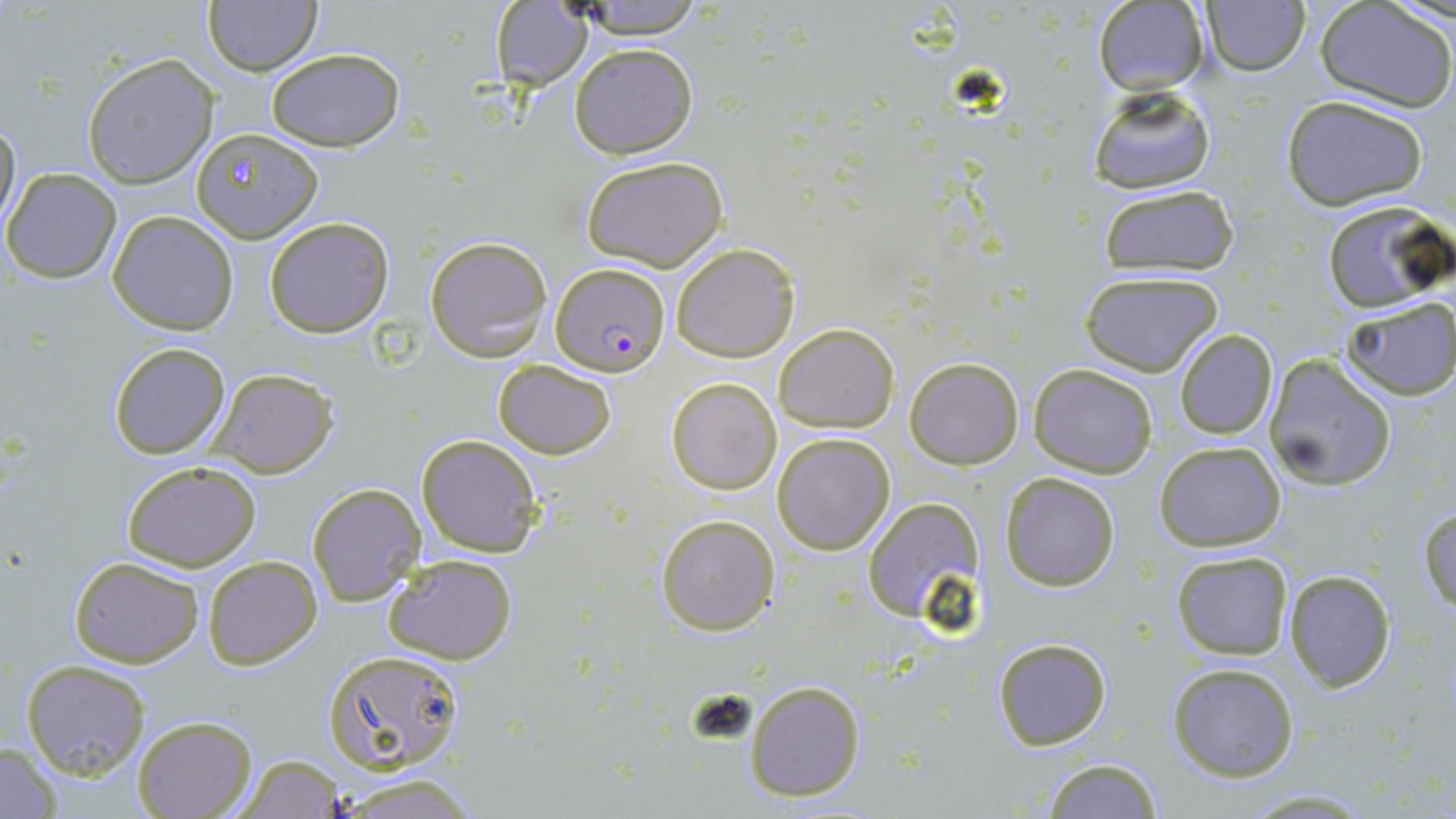
Approximate bounding boxes as [x1, y1, x2, y2] in pixels. Plasmodium falciparum-infected red blood cell locations: [548, 263, 669, 375]. Uninfected red blood cell locations: [1202, 0, 1308, 75], [203, 1, 321, 75], [570, 1, 709, 42], [489, 2, 594, 90], [1093, 2, 1210, 96], [1315, 2, 1454, 112], [570, 43, 698, 159], [263, 47, 408, 149], [83, 55, 218, 189], [1090, 86, 1215, 194], [1281, 94, 1430, 209], [0, 112, 21, 235], [190, 127, 321, 242], [581, 155, 730, 272], [2, 169, 121, 283], [1098, 182, 1240, 274], [1320, 200, 1450, 314], [107, 210, 239, 335], [263, 215, 395, 338], [425, 236, 551, 362], [672, 242, 800, 363], [1080, 271, 1224, 376], [1341, 298, 1456, 400], [774, 322, 900, 433], [1175, 329, 1277, 439], [106, 343, 231, 459], [1264, 353, 1396, 492], [906, 356, 1023, 469], [491, 357, 617, 459], [1029, 364, 1157, 478], [208, 367, 338, 477], [666, 377, 781, 495], [771, 432, 896, 555], [415, 434, 542, 558], [1154, 441, 1285, 551], [119, 460, 263, 569], [1000, 472, 1121, 591], [306, 482, 426, 608], [863, 497, 985, 625], [1419, 505, 1455, 613], [656, 513, 779, 636], [1170, 549, 1294, 660], [381, 554, 518, 663], [202, 555, 322, 669], [67, 556, 204, 668], [1283, 568, 1396, 692], [991, 638, 1112, 752], [322, 648, 468, 775], [20, 660, 152, 779], [1167, 661, 1301, 783], [744, 678, 867, 803], [133, 716, 255, 819], [0, 741, 63, 817], [231, 752, 347, 817], [1040, 758, 1165, 818], [325, 773, 490, 817], [1237, 789, 1379, 817]. Slide-level diagnosis: Plasmodium falciparum. May-Grünwald-Giemsa-stained preparation. 1000x magnification. Thin blood smear. One field of a larger specimen. Optical microscopy. Image is 1456×819 pixels.